Report the malaria status of this cell.
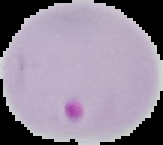
Parasitized.

From a thin blood film. Image is 163×145 pixels. The area outside the segmented cell region is set to black.